Look for Plasmodium parasites.
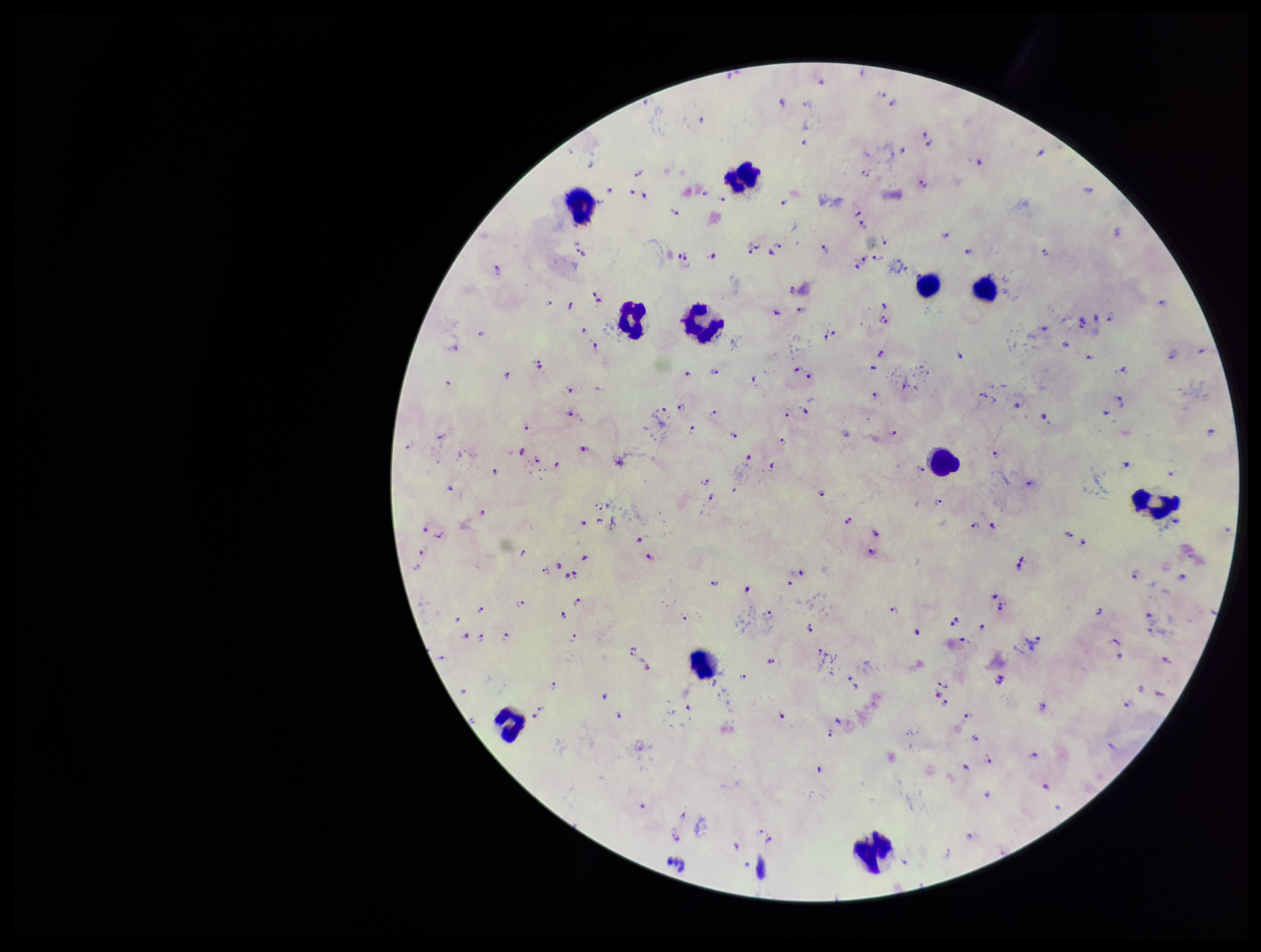
Detected.

Summary:
  - Field of view: single
  - Patient malaria status: positive
  - Image size: 1261×952 pixels
  - Species reported for this patient: Plasmodium falciparum
  - Leukocyte count: 11
  - Capture: smartphone photograph through the microscope eyepiece
  - Preparation: thick smear
  - Parasite count: 169
  - Stain: Giemsa